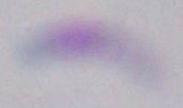

magnification: 1000x
identification: Toxoplasma gondii
modality: photomicrograph